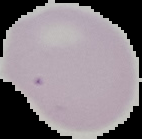
Summary:
  - Preparation: thin blood smear
  - Image size: 142×139 pixels
  - Image type: segmented cell region with the area outside set to black
  - Result: negative for malaria parasites